Report the malaria status.
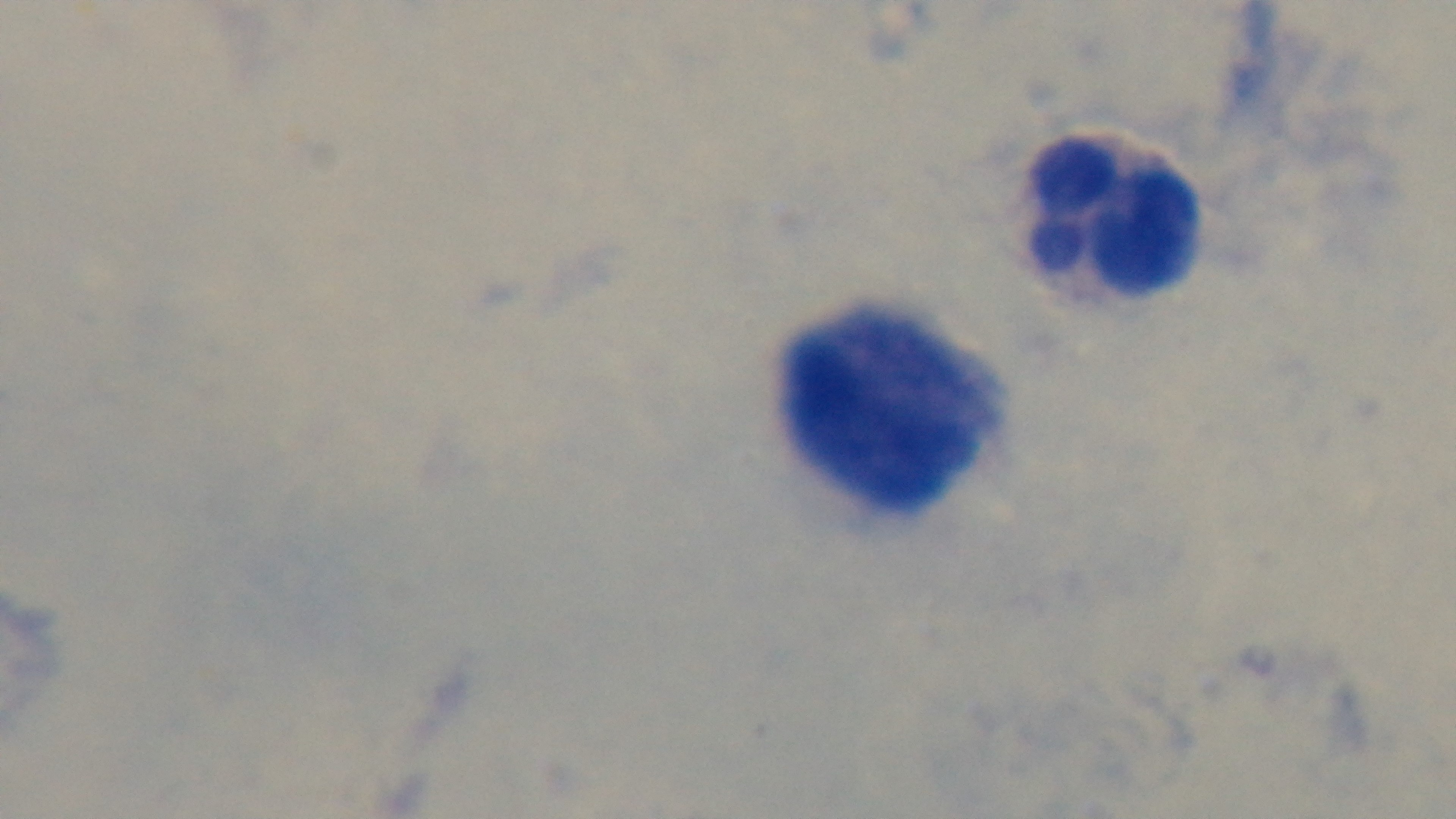

Negative.

Giemsa-stained. Preparation: thick. Mounted 4K digital camera. Oil-immersion objective, 100x. Single field of view. Light microscopy.